Comment on the morphology of the red blood cells.
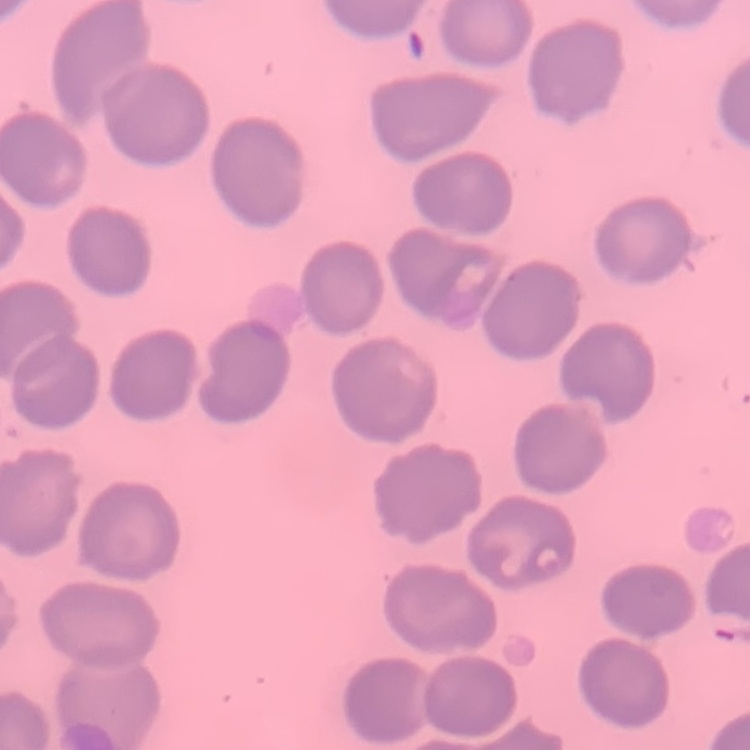
They show no rouleaux formation.

image_type: square crop of a larger photomicrograph
stain: Field's or Giemsa
preparation: thin blood film